Name the parasite shown.
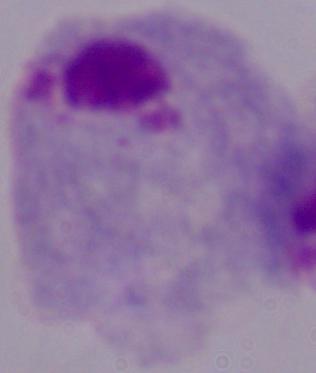

A trichomonad.

Captured at 1000x magnification. Micrograph.